Assess this cell for malaria.
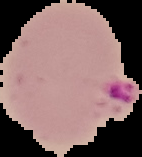
Parasitized.

From a thin blood film. Segmented cell region on a black background. Image is 142×157 pixels.